Comment on the morphology of the red blood cells.
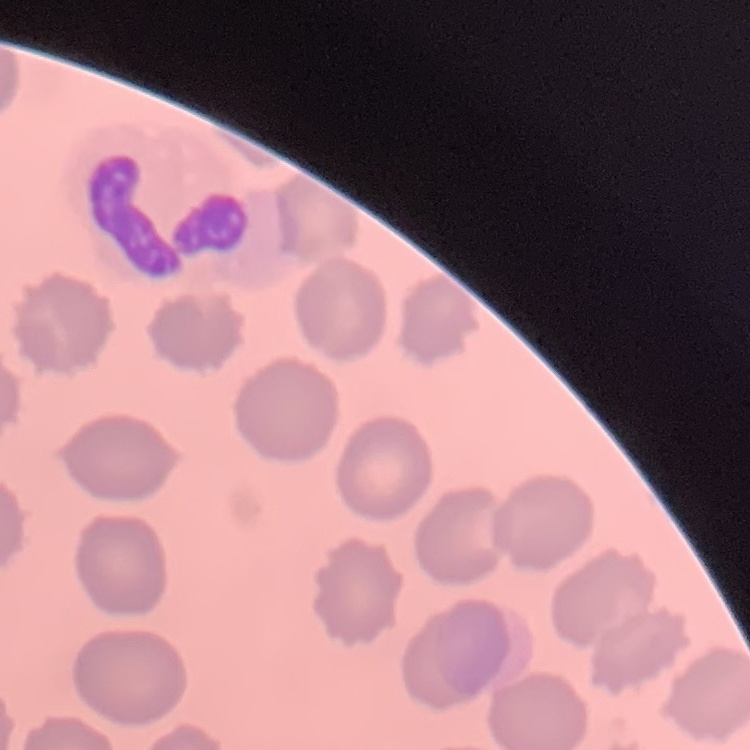

They show no rouleaux formation.

stain = Field's or Giemsa
image type = square crop of a larger photomicrograph
preparation = thin peripheral smear